Classify this cell by malaria status.
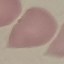
It is uninfected.

Summary:
  - Capture: smartphone camera at the microscope eyepiece
  - Image type: automatically extracted cell patch, resized to 64 × 64 pixels
  - Stain: Giemsa
  - Preparation: thin smear